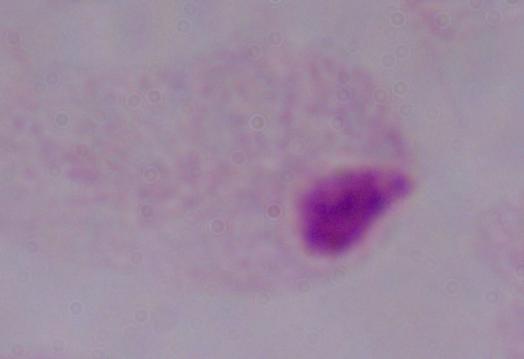

A trichomonad is shown. 1000x magnification. Micrograph.